Assess this cell for malaria.
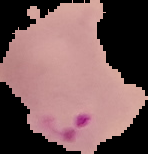
Parasitized.

Summary:
  - Image type: segmented cell region with the area outside set to black
  - Preparation: thin blood smear
  - Image size: 148×154 pixels